State which cell type is depicted.
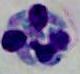

This is a leukocyte.

modality: micrograph
magnification: 1000x